Name the parasite shown.
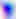
This is Toxoplasma gondii.

400x magnification. Micrograph.